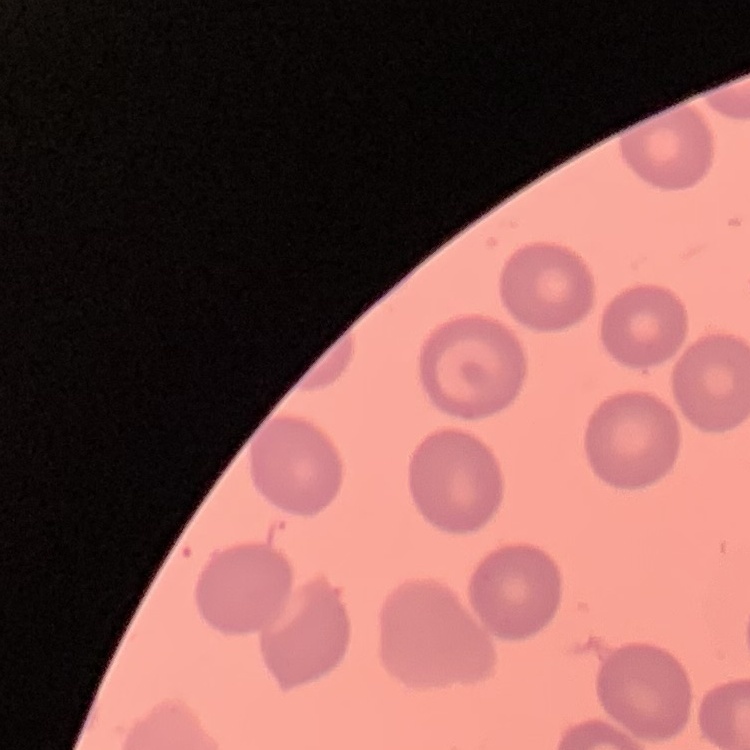

erythrocyte morphology = no rouleaux formation
preparation = thin blood smear
stain = Field's or Giemsa
image type = one tile cut from a larger photomicrograph